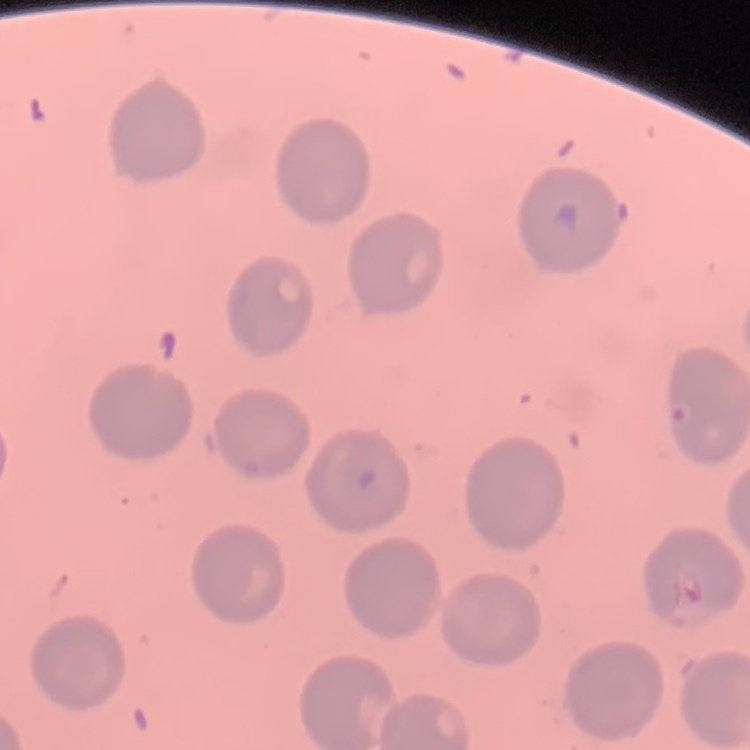
red_blood_cell_morphology: no rouleaux formation
preparation: thin blood smear
stain: Field's or Giemsa
image_type: one tile cut from a larger photomicrograph